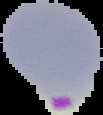
{
  "preparation": "thin blood film",
  "malaria_status": "parasitized",
  "image_type": "cell region segmented out of the field of view; surrounding area masked to black",
  "image_size": "103×115 pixels"
}